Report the malaria status of this cell.
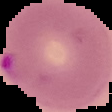
It is parasitized.

{
  "image_size": "112×112 pixels",
  "preparation": "thin blood film",
  "image_type": "segmented cell region with the area outside set to black"
}